Report the malaria status of this cell.
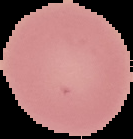
Uninfected.

Summary:
  - Image size: 133×139 pixels
  - Image type: segmented cell region with the area outside set to black
  - Preparation: thin blood smear